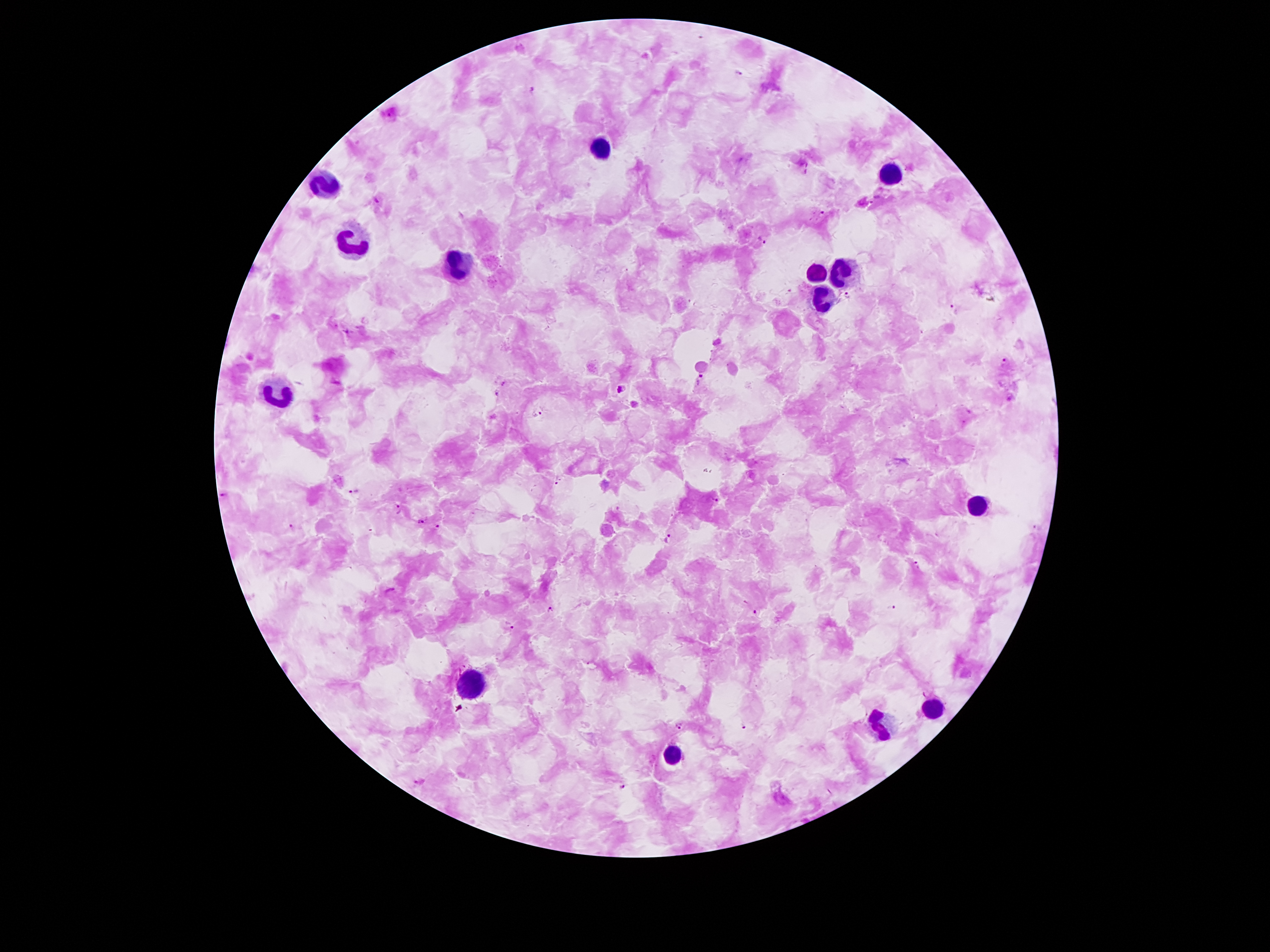

Approximate centers as [x, y] in pixels.
Summary:
  - Leukocyte locations: [601, 145], [893, 172], [326, 181], [349, 244], [454, 261], [817, 270], [845, 273], [818, 297], [280, 396], [977, 508], [469, 679], [933, 712], [880, 723], [673, 752]
  - Malaria parasite locations: [737, 71], [532, 89], [808, 168], [376, 201], [822, 213], [761, 240], [848, 294], [954, 308], [1004, 363], [701, 380], [502, 383], [621, 387], [542, 410], [557, 481], [351, 492], [223, 494], [716, 500], [397, 508], [420, 522], [290, 527], [438, 527], [668, 538], [915, 566], [390, 590], [892, 608], [550, 610], [755, 611], [510, 625], [679, 726], [743, 726], [421, 782], [624, 787]
  - Capture: smartphone camera through the microscope eyepiece
  - Preparation: thick peripheral-blood smear
  - Field of view: single
  - Image size: 1270×952 pixels
  - Stain: Giemsa
  - Magnification: 100x
  - Patient malaria status: positive for Plasmodium falciparum